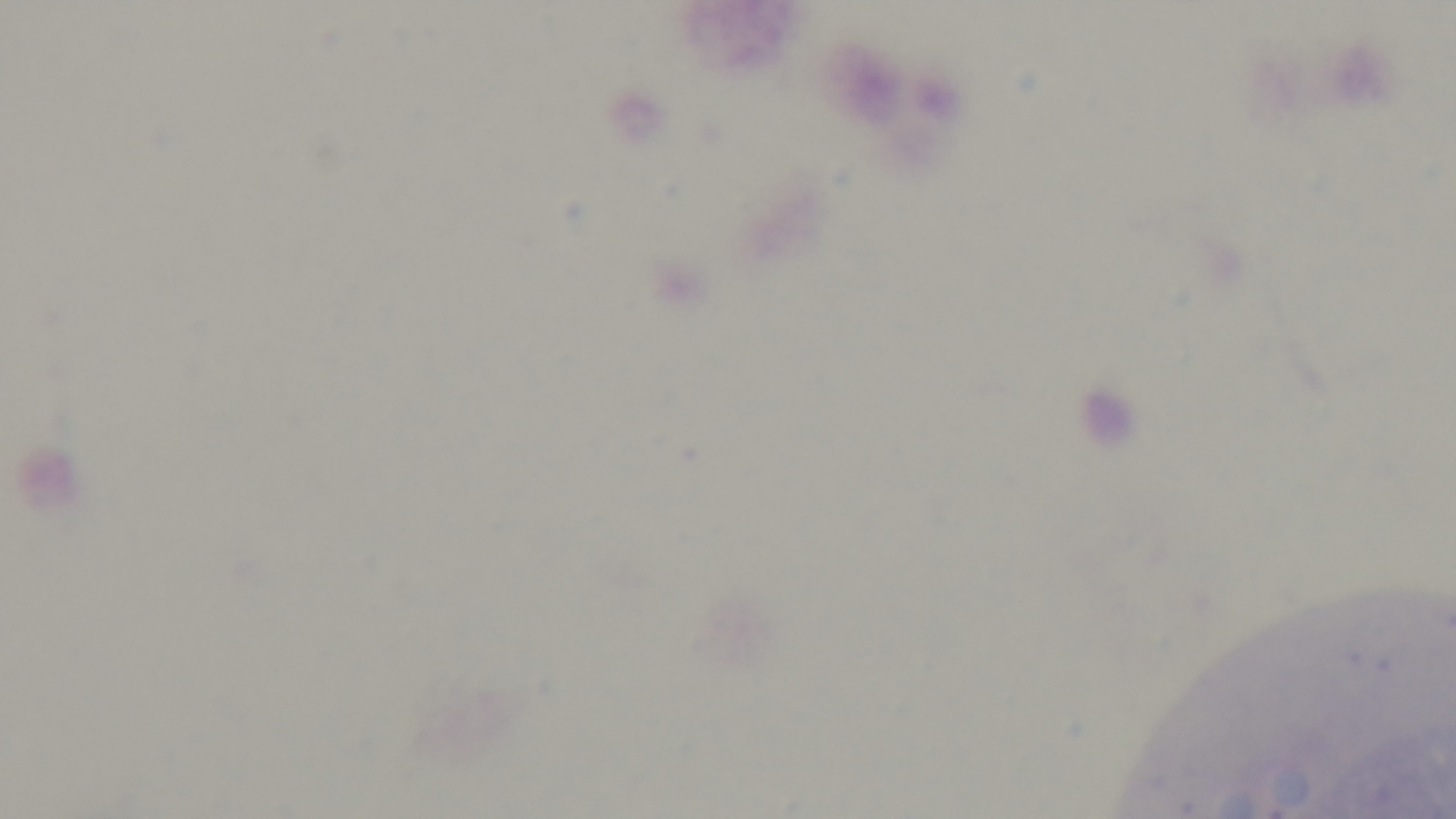

malaria_status: uninfected
stain: Giemsa
modality: light microscopy
capture: mounted 4K digital camera
objective: 100x oil immersion
field_of_view: one from the slide
preparation: thick smear